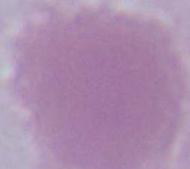

1000x magnification. Photomicrograph. An erythrocyte is shown.